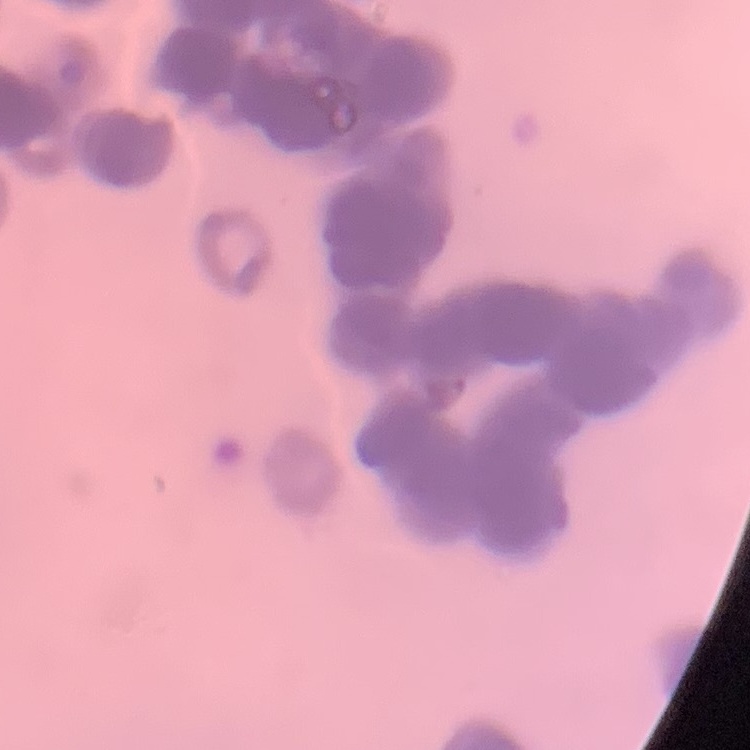 The erythrocytes exhibit rouleaux formation. Square crop of a larger photomicrograph. Thin blood film. Field's or Giemsa stain.